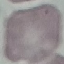
malaria_status: uninfected
preparation: thin blood smear
stain: Giemsa
image_type: cell patch, automatically extracted from a larger field of view and resized to 64 × 64 pixels
capture: smartphone camera at the microscope eyepiece